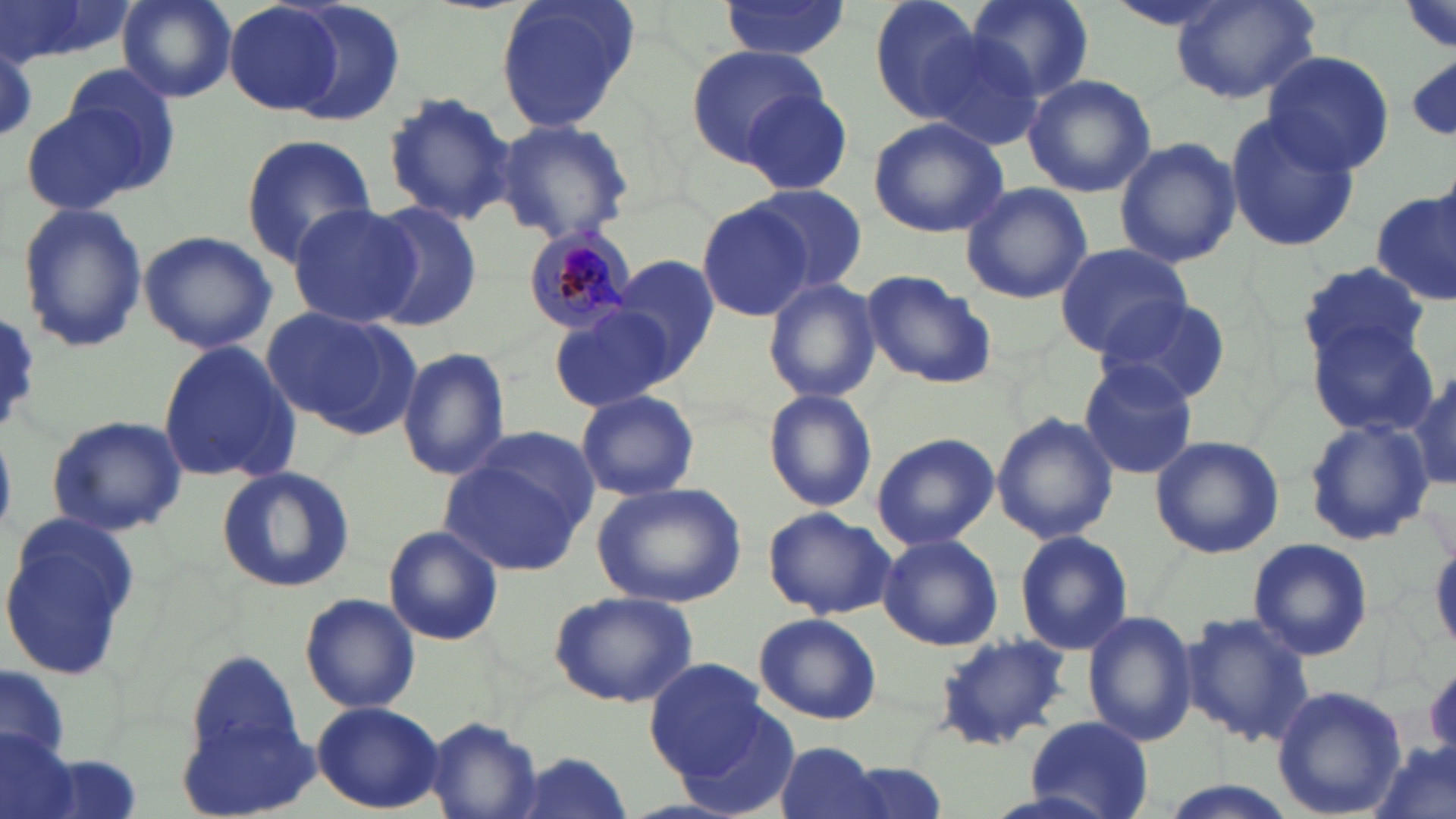

Approximate bounding boxes as (x1, y1, x2, y2) in pixels. Plasmodium malariae-infected red blood cell locations: (520, 222, 639, 336). Uninfected red blood cell locations: (0, 0, 134, 69), (117, 0, 237, 103), (270, 0, 408, 128), (495, 0, 638, 135), (865, 0, 987, 120), (963, 0, 1094, 105), (1103, 0, 1243, 34), (1172, 0, 1318, 105), (716, 1, 850, 59), (224, 2, 345, 117), (913, 27, 1043, 151), (0, 41, 37, 145), (684, 44, 829, 165), (1262, 49, 1394, 175), (55, 63, 180, 193), (1022, 73, 1156, 197), (737, 88, 855, 194), (381, 89, 517, 226), (22, 104, 150, 216), (1224, 112, 1359, 252), (868, 116, 1011, 239), (493, 118, 637, 246), (239, 133, 379, 267), (1112, 136, 1242, 268), (959, 182, 1092, 305), (747, 184, 868, 294), (1373, 190, 1455, 308), (698, 200, 812, 320), (364, 201, 480, 332), (286, 202, 417, 330), (17, 203, 149, 352), (136, 230, 278, 353), (1053, 243, 1192, 356), (613, 255, 721, 377), (1301, 262, 1428, 365), (862, 271, 996, 389), (765, 279, 881, 404), (1096, 293, 1234, 406), (551, 303, 677, 413), (261, 306, 416, 434), (0, 313, 46, 436), (1309, 321, 1441, 437), (155, 340, 299, 485), (397, 348, 511, 481), (1079, 360, 1199, 478), (1406, 361, 1456, 498), (764, 389, 878, 512), (576, 390, 699, 500), (990, 413, 1119, 544), (45, 417, 189, 537), (1303, 420, 1433, 546), (871, 433, 998, 551), (1149, 434, 1285, 559), (441, 441, 595, 576), (215, 464, 355, 594), (590, 482, 747, 608), (763, 506, 894, 619), (0, 524, 142, 679), (382, 526, 504, 646), (1014, 531, 1133, 655), (877, 533, 1003, 651), (1246, 537, 1375, 662), (548, 590, 698, 708), (300, 592, 420, 713), (1082, 609, 1200, 746), (1179, 609, 1317, 751), (754, 612, 882, 725), (932, 634, 1072, 751), (187, 653, 304, 769), (645, 660, 776, 783), (1, 667, 70, 762), (1267, 681, 1410, 818), (311, 701, 444, 812), (671, 705, 802, 819), (424, 716, 544, 818), (1024, 716, 1154, 818), (0, 730, 80, 819), (1367, 739, 1454, 819), (772, 741, 890, 819), (505, 751, 637, 818), (828, 757, 949, 819), (1158, 781, 1294, 819). Slide-level diagnosis: Plasmodium malariae. Thin blood film. Optical microscopy. Single field of view. May-Grünwald-Giemsa stain. Captured at 1000x magnification. Image is 1456×819 pixels.